State which parasite is depicted.
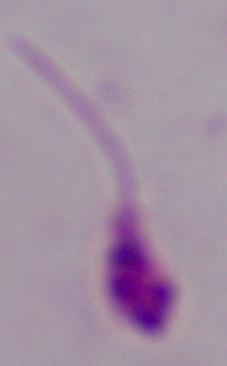

Leishmania.

Summary:
  - Magnification: 1000x
  - Modality: micrograph